Name the parasite shown.
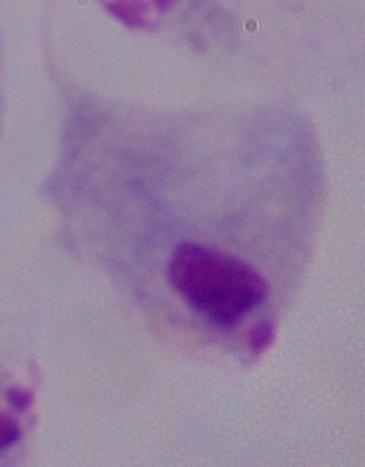

A trichomonad.

1000x magnification. Photomicrograph.